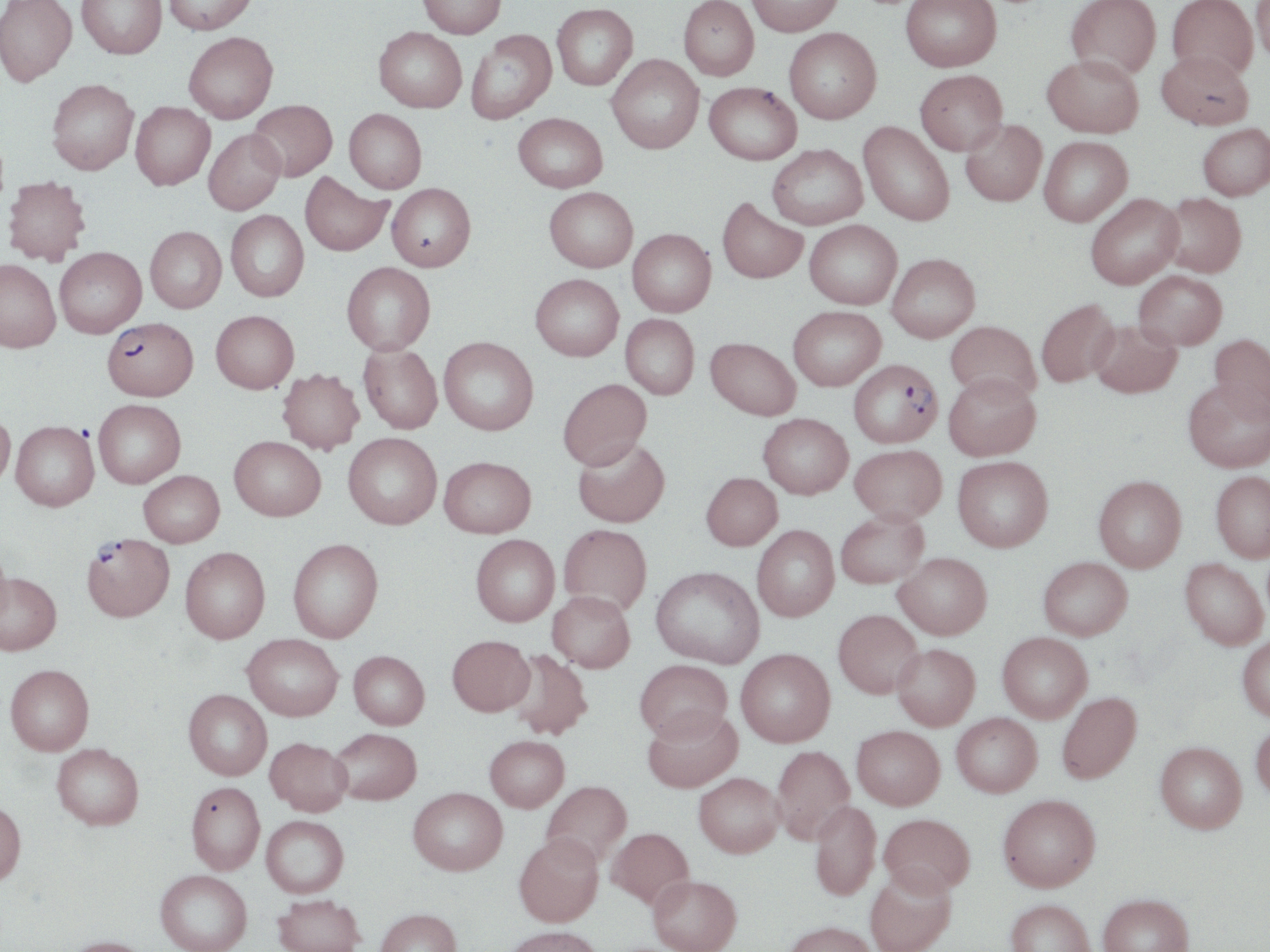
Summary:
  - Coordinate format: approximate bounding boxes as (x1,y1)-(x2,y2) corner pairs in pixels
  - Plasmodium falciparum-infected red blood cell locations: (102,317)-(198,401), (847,358)-(943,449), (82,532)-(174,621)
  - Uninfected red blood cell locations: (0,0)-(77,86), (77,0)-(167,58), (163,0)-(258,35), (417,0)-(506,38), (678,0)-(759,81), (747,0)-(842,36), (900,0)-(1001,72), (1066,0)-(1162,79), (1167,0)-(1258,79), (1252,1)-(1270,63), (552,3)-(638,90), (374,27)-(466,112), (784,28)-(882,124), (466,30)-(556,123), (183,32)-(278,123), (1157,50)-(1253,130), (606,54)-(704,154), (1043,54)-(1143,137), (915,69)-(1007,155), (46,79)-(139,174), (704,82)-(802,165), (248,99)-(337,181), (130,101)-(215,190), (344,108)-(426,193), (513,112)-(607,192), (960,120)-(1047,206), (858,122)-(954,225), (1198,123)-(1270,200), (204,128)-(286,214), (1039,136)-(1132,226), (767,144)-(867,229), (300,172)-(392,256), (3,176)-(91,265), (387,183)-(476,271), (544,187)-(638,272), (1159,192)-(1246,277), (1085,193)-(1183,289), (717,197)-(808,283), (225,211)-(309,301), (804,220)-(902,309), (145,226)-(226,313), (627,229)-(716,317), (54,246)-(146,337), (887,253)-(980,342), (0,259)-(60,352), (342,262)-(435,355), (1134,270)-(1227,350), (530,274)-(624,361), (1036,299)-(1120,387), (788,305)-(886,390), (211,310)-(299,393), (621,314)-(699,399), (1090,319)-(1182,398), (945,320)-(1041,403), (1209,333)-(1270,422), (439,336)-(538,435), (705,337)-(800,420), (359,344)-(442,434), (277,368)-(364,454), (943,373)-(1040,460), (558,378)-(652,470), (1184,378)-(1270,472), (93,399)-(185,488), (0,410)-(15,490), (758,413)-(853,498), (11,421)-(98,511), (343,432)-(442,529), (229,436)-(325,520), (572,436)-(670,527), (850,444)-(946,524), (439,456)-(536,538), (953,456)-(1053,552), (138,470)-(224,547), (1211,471)-(1270,561), (701,472)-(782,550), (1093,475)-(1187,572), (836,510)-(929,588), (559,523)-(652,615), (752,525)-(840,622), (471,534)-(559,626), (288,538)-(383,643), (180,547)-(270,643), (0,549)-(13,631), (894,552)-(992,639), (1038,556)-(1132,640), (1180,558)-(1268,650), (651,566)-(764,668), (0,573)-(62,655), (547,591)-(635,672), (833,609)-(924,698), (997,632)-(1092,722), (242,634)-(343,720), (447,635)-(535,716), (1237,635)-(1270,722), (892,644)-(980,730), (505,649)-(593,740), (736,649)-(835,747), (349,650)-(429,729), (635,659)-(732,742), (5,664)-(94,755), (184,690)-(272,780), (1056,691)-(1142,784), (643,708)-(742,793), (951,712)-(1042,797), (1250,718)-(1270,801), (852,725)-(945,810), (330,727)-(421,805), (485,735)-(569,811), (265,737)-(352,816), (1155,741)-(1246,834), (52,744)-(144,830), (771,745)-(854,844), (693,772)-(784,857), (541,780)-(632,866), (186,781)-(265,874), (408,787)-(508,875), (998,794)-(1101,891), (810,800)-(880,901), (0,801)-(26,886), (879,813)-(975,896), (261,815)-(349,897), (607,827)-(694,909), (514,833)-(603,927), (865,867)-(956,952), (155,870)-(251,952), (648,875)-(742,952), (1098,893)-(1194,952), (273,894)-(365,952), (1006,899)-(1097,952), (374,908)-(462,952), (783,920)-(878,952), (503,926)-(604,952), (62,936)-(154,952)
  - Slide-level diagnosis: Plasmodium falciparum
  - Stain: May-Grünwald-Giemsa
  - Image size: 1270×952 pixels
  - Field of view: one of a larger specimen
  - Modality: optical microscopy
  - Magnification: 1000x
  - Preparation: thin blood film